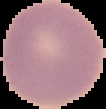
From a thin blood film. Image is 106×109 pixels. Segmented cell region on a black background. Result: negative for malaria parasites.